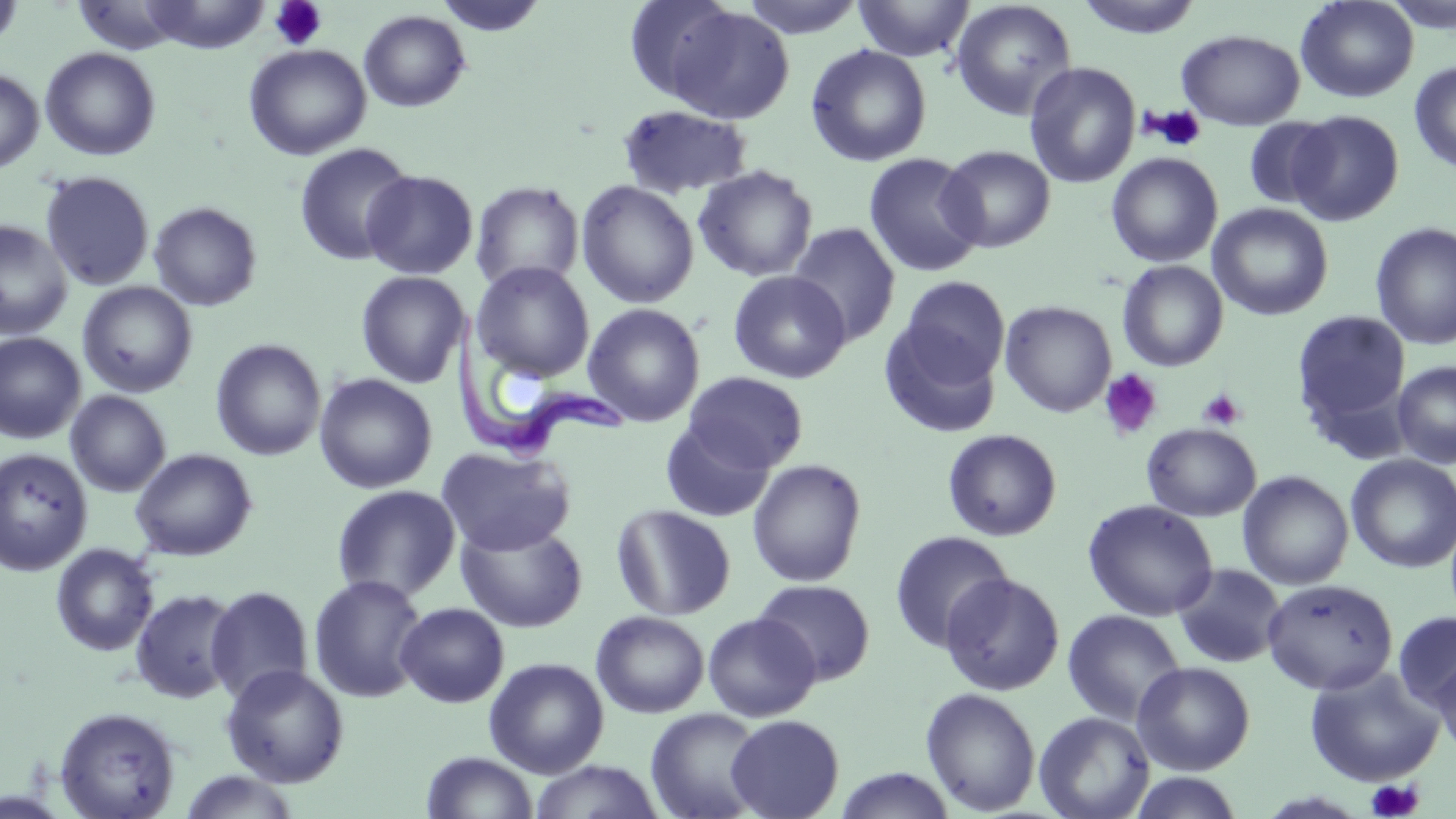

Approximate bounding boxes as named x1/y1/x2/y2 corners in pixels. Trypanosoma brucei locations: (x1=448, y1=304, x2=627, y2=465). Uninfected red blood cell locations: (x1=0, y1=0, x2=24, y2=52), (x1=433, y1=0, x2=549, y2=37), (x1=622, y1=0, x2=741, y2=103), (x1=738, y1=0, x2=868, y2=38), (x1=852, y1=0, x2=974, y2=62), (x1=1075, y1=0, x2=1205, y2=40), (x1=1295, y1=0, x2=1419, y2=103), (x1=139, y1=1, x2=272, y2=52), (x1=949, y1=1, x2=1077, y2=121), (x1=663, y1=6, x2=795, y2=126), (x1=358, y1=10, x2=471, y2=113), (x1=1176, y1=28, x2=1305, y2=130), (x1=243, y1=43, x2=371, y2=160), (x1=806, y1=44, x2=932, y2=166), (x1=40, y1=47, x2=161, y2=161), (x1=1024, y1=61, x2=1141, y2=188), (x1=1409, y1=62, x2=1456, y2=173), (x1=0, y1=68, x2=44, y2=174), (x1=617, y1=104, x2=753, y2=199), (x1=1288, y1=110, x2=1405, y2=226), (x1=1242, y1=117, x2=1339, y2=210), (x1=294, y1=143, x2=415, y2=266), (x1=938, y1=145, x2=1056, y2=253), (x1=863, y1=152, x2=985, y2=277), (x1=1105, y1=152, x2=1223, y2=267), (x1=692, y1=165, x2=818, y2=282), (x1=361, y1=169, x2=479, y2=280), (x1=40, y1=170, x2=155, y2=290), (x1=470, y1=180, x2=584, y2=292), (x1=576, y1=180, x2=699, y2=309), (x1=148, y1=201, x2=263, y2=311), (x1=1208, y1=202, x2=1334, y2=321), (x1=0, y1=220, x2=73, y2=339), (x1=1370, y1=221, x2=1456, y2=351), (x1=786, y1=222, x2=901, y2=347), (x1=1117, y1=260, x2=1229, y2=371), (x1=471, y1=261, x2=595, y2=382), (x1=355, y1=270, x2=471, y2=388), (x1=727, y1=270, x2=851, y2=383), (x1=899, y1=276, x2=1010, y2=384), (x1=77, y1=281, x2=198, y2=398), (x1=1000, y1=300, x2=1117, y2=417), (x1=583, y1=303, x2=705, y2=427), (x1=1292, y1=309, x2=1411, y2=434), (x1=879, y1=324, x2=1001, y2=439), (x1=0, y1=332, x2=86, y2=444), (x1=210, y1=338, x2=327, y2=460), (x1=1392, y1=361, x2=1456, y2=468), (x1=683, y1=371, x2=808, y2=472), (x1=314, y1=373, x2=438, y2=493), (x1=66, y1=390, x2=171, y2=497), (x1=660, y1=418, x2=775, y2=523), (x1=1141, y1=422, x2=1262, y2=521), (x1=942, y1=428, x2=1062, y2=541), (x1=437, y1=446, x2=575, y2=556), (x1=0, y1=447, x2=93, y2=576), (x1=129, y1=447, x2=258, y2=561), (x1=1345, y1=454, x2=1456, y2=573), (x1=747, y1=459, x2=867, y2=586), (x1=1237, y1=471, x2=1353, y2=589), (x1=332, y1=485, x2=462, y2=602), (x1=1082, y1=499, x2=1219, y2=621), (x1=611, y1=504, x2=736, y2=621), (x1=455, y1=520, x2=589, y2=633), (x1=889, y1=530, x2=1014, y2=653), (x1=50, y1=543, x2=159, y2=656), (x1=1172, y1=563, x2=1287, y2=669), (x1=940, y1=572, x2=1065, y2=696), (x1=308, y1=574, x2=429, y2=703), (x1=752, y1=578, x2=876, y2=686), (x1=1261, y1=578, x2=1398, y2=695), (x1=204, y1=585, x2=314, y2=705), (x1=129, y1=587, x2=242, y2=704), (x1=395, y1=602, x2=509, y2=708), (x1=1061, y1=609, x2=1187, y2=726), (x1=591, y1=610, x2=710, y2=718), (x1=1393, y1=610, x2=1456, y2=713), (x1=703, y1=612, x2=821, y2=721), (x1=1433, y1=650, x2=1456, y2=759), (x1=483, y1=657, x2=609, y2=778), (x1=1132, y1=661, x2=1255, y2=775), (x1=221, y1=663, x2=350, y2=788), (x1=1304, y1=664, x2=1444, y2=787), (x1=920, y1=687, x2=1041, y2=816), (x1=53, y1=705, x2=181, y2=819), (x1=645, y1=707, x2=767, y2=819), (x1=1034, y1=711, x2=1155, y2=819), (x1=726, y1=714, x2=844, y2=818), (x1=420, y1=751, x2=539, y2=818), (x1=527, y1=760, x2=665, y2=819), (x1=833, y1=768, x2=957, y2=819), (x1=177, y1=770, x2=302, y2=818), (x1=1126, y1=770, x2=1247, y2=818). Platelet locations: (x1=269, y1=1, x2=328, y2=51), (x1=1143, y1=105, x2=1207, y2=151), (x1=1099, y1=369, x2=1163, y2=441), (x1=1197, y1=389, x2=1246, y2=430), (x1=1366, y1=779, x2=1425, y2=818). Slide-level diagnosis: Trypanosoma brucei. Light microscopy. May-Grünwald-Giemsa-stained preparation. 1000x magnification. One field of a larger specimen. Thin blood smear. Image is 1456×819 pixels.